Mark where platelets are.
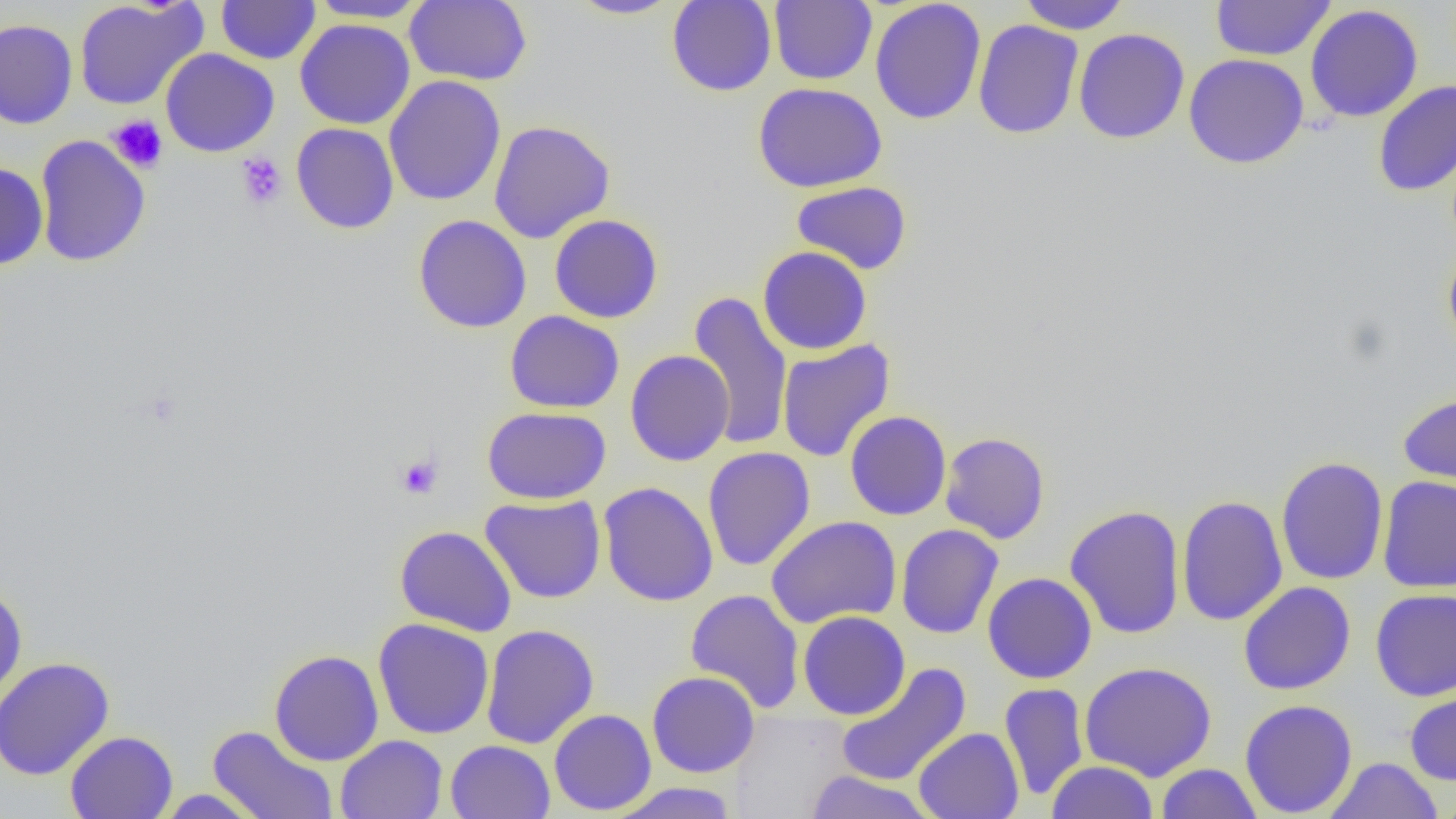
Approximate bounding boxes as (x1, y1, x2, y2) in pixels.
Platelets: (107, 115, 168, 172), (236, 152, 287, 209), (395, 454, 443, 499).

Uninfected red blood cell locations: (74, 0, 208, 110), (216, 0, 321, 64), (305, 0, 432, 23), (404, 0, 533, 86), (567, 0, 681, 20), (666, 0, 777, 97), (769, 0, 877, 85), (870, 0, 986, 125), (1017, 0, 1131, 34), (1211, 1, 1336, 61), (1305, 4, 1423, 123), (0, 18, 78, 130), (295, 18, 415, 130), (973, 19, 1084, 139), (1073, 28, 1190, 144), (160, 48, 279, 157), (1184, 53, 1309, 169), (384, 75, 506, 206), (1373, 80, 1456, 197), (753, 81, 888, 192), (488, 120, 615, 243), (291, 122, 399, 234), (34, 135, 151, 267), (0, 162, 48, 270), (791, 181, 913, 274), (413, 214, 532, 333), (549, 214, 663, 323), (1442, 243, 1456, 355), (758, 246, 872, 355), (687, 290, 792, 451), (504, 310, 624, 413), (777, 339, 895, 462), (625, 350, 734, 466), (1397, 393, 1456, 492), (482, 406, 611, 504), (845, 410, 951, 520), (940, 431, 1051, 544), (703, 446, 815, 571), (1275, 456, 1389, 585), (1377, 476, 1456, 593), (598, 481, 718, 607), (480, 494, 606, 603), (1175, 495, 1287, 626), (1064, 505, 1185, 639), (766, 515, 902, 629), (896, 524, 1004, 639), (394, 525, 518, 637), (982, 572, 1097, 684), (1239, 581, 1356, 695), (0, 584, 28, 704), (685, 588, 805, 714), (1370, 588, 1456, 701), (798, 610, 910, 720), (373, 618, 495, 739), (666, 619, 782, 766), (481, 624, 599, 749), (269, 649, 384, 766), (0, 657, 115, 781), (1080, 660, 1218, 781), (834, 663, 972, 787), (647, 671, 760, 777), (999, 682, 1089, 802), (1404, 684, 1456, 786), (1240, 699, 1358, 818), (549, 709, 656, 815), (207, 725, 340, 819), (913, 727, 1024, 819), (65, 730, 178, 819), (336, 734, 447, 819), (446, 740, 555, 819), (1323, 757, 1443, 818), (1046, 760, 1158, 819), (1155, 763, 1263, 819), (804, 770, 936, 819), (607, 782, 740, 818), (1433, 786, 1456, 819), (154, 789, 268, 818). Slide-level diagnosis: no evidence of blood parasites. Thin blood film. Captured at 1000x magnification. Image is 1456×819 pixels. Single field of view. Optical microscopy.